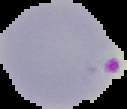

image type = segmented cell region with the area outside set to black
image size = 127×109 pixels
malaria status = parasitized
preparation = thin blood smear